Outline each Plasmodium vivax-infected red blood cell.
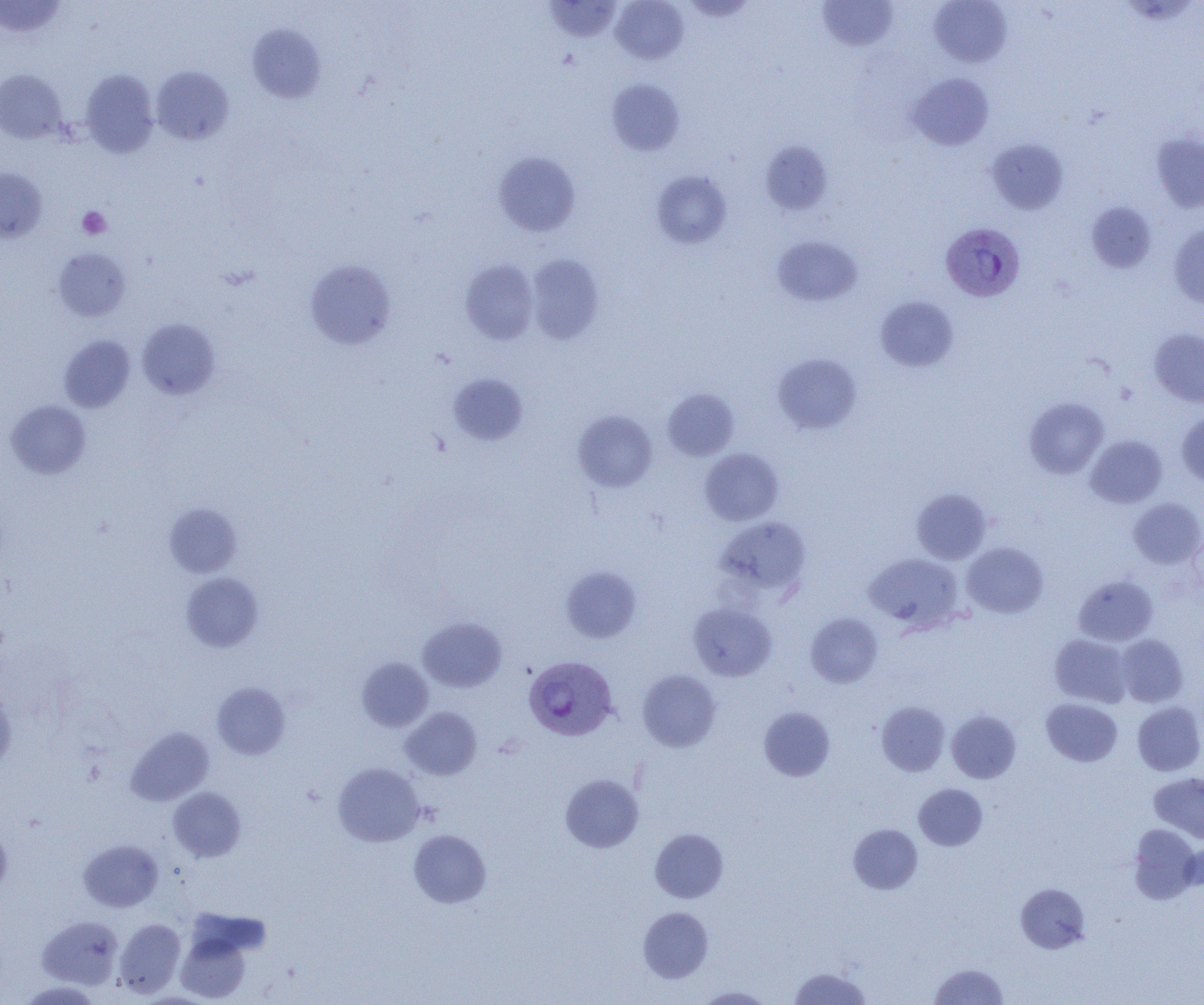

Approximate bounding boxes as [x1, y1, x2, y2] in pixels.
Plasmodium vivax-infected red blood cells: [942, 229, 1025, 302], [524, 656, 618, 741].

Summary:
  - Platelet locations: [77, 206, 111, 240]
  - Uninfected red blood cell locations: [544, 0, 621, 41], [611, 0, 689, 64], [681, 0, 756, 22], [816, 0, 898, 51], [929, 0, 1012, 67], [0, 1, 67, 38], [246, 22, 326, 103], [151, 66, 233, 145], [0, 69, 68, 144], [80, 70, 159, 158], [906, 73, 994, 150], [606, 78, 684, 156], [1151, 132, 1204, 213], [986, 138, 1069, 214], [760, 140, 833, 215], [494, 150, 580, 236], [0, 167, 48, 241], [652, 170, 731, 249], [1085, 202, 1156, 272], [1169, 224, 1204, 310], [772, 235, 862, 306], [52, 247, 131, 321], [527, 254, 604, 344], [305, 259, 397, 350], [460, 259, 539, 344], [876, 295, 959, 371], [137, 318, 220, 399], [1149, 328, 1204, 407], [59, 334, 135, 412], [772, 353, 862, 434], [448, 373, 528, 445], [662, 388, 740, 461], [1024, 397, 1108, 479], [6, 400, 91, 478], [573, 410, 657, 492], [1176, 411, 1204, 486], [1086, 435, 1167, 508], [700, 449, 783, 525], [911, 488, 992, 564], [1129, 497, 1204, 568], [164, 502, 242, 577], [715, 517, 811, 600], [962, 542, 1048, 618], [864, 554, 963, 631], [560, 566, 642, 643], [181, 572, 263, 652], [1073, 575, 1158, 646], [688, 602, 776, 681], [805, 612, 883, 688], [418, 617, 507, 692], [1050, 633, 1133, 708], [1116, 634, 1188, 707], [356, 657, 433, 732], [637, 669, 722, 752], [212, 681, 290, 759], [0, 684, 17, 769], [1041, 698, 1122, 767], [877, 701, 950, 776], [1132, 701, 1204, 775], [758, 706, 835, 781], [401, 707, 482, 780], [947, 710, 1021, 783], [125, 726, 214, 806], [333, 762, 425, 847], [1149, 772, 1204, 843], [560, 774, 644, 853], [913, 783, 988, 850], [169, 787, 246, 862], [0, 824, 11, 898], [848, 824, 922, 894], [1129, 824, 1200, 904], [650, 828, 728, 903], [408, 829, 491, 908], [79, 839, 163, 911], [1182, 839, 1204, 893], [1015, 883, 1090, 953], [638, 906, 713, 983], [37, 915, 124, 989], [114, 918, 185, 997], [176, 925, 254, 1003], [929, 963, 1008, 1005], [788, 967, 872, 1005], [694, 986, 775, 1004]
  - Slide-level diagnosis: Plasmodium vivax
  - Image size: 1204×1005 pixels
  - Modality: optical microscopy
  - Magnification: 1000x
  - Preparation: thin blood smear
  - Field of view: one of a larger specimen